Locate every blood parasite and identify its species.
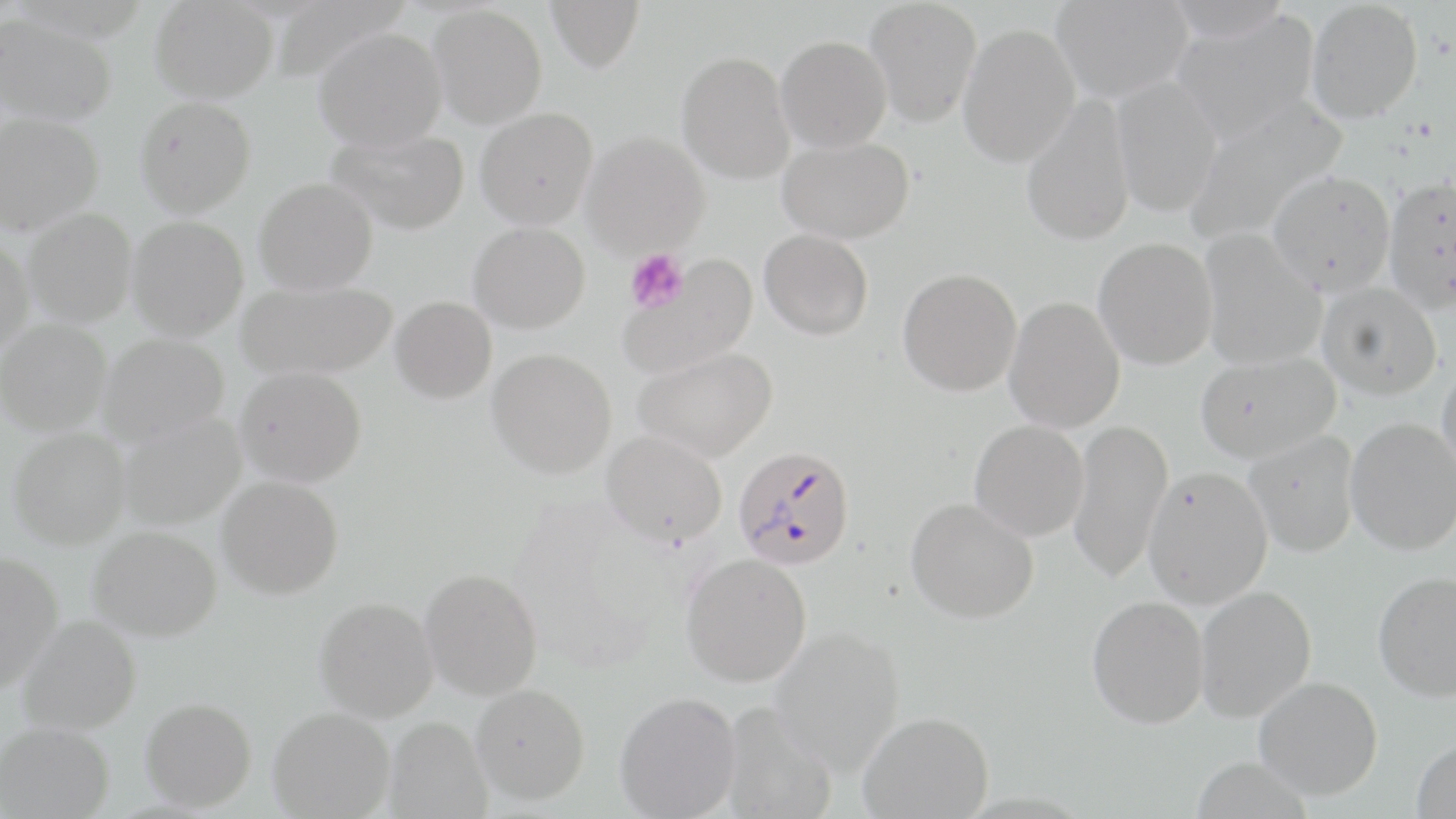

Approximate bounding boxes as [x1, y1, x2, y2] in pixels.
Plasmodium falciparum-infected red blood cells: [733, 445, 855, 570].
No Plasmodium ovale, Plasmodium malariae, Plasmodium vivax, Babesia divergens, or Trypanosoma brucei observed.

Uninfected red blood cell locations: [149, 0, 278, 101], [545, 0, 645, 73], [865, 0, 982, 128], [1052, 0, 1192, 101], [1165, 0, 1293, 41], [1306, 1, 1423, 123], [428, 4, 547, 128], [1171, 9, 1319, 142], [0, 14, 117, 126], [958, 22, 1081, 167], [313, 27, 447, 151], [776, 35, 892, 152], [677, 51, 795, 184], [1111, 77, 1223, 217], [1020, 95, 1136, 247], [135, 96, 256, 217], [1182, 98, 1348, 245], [475, 107, 598, 230], [0, 112, 103, 235], [326, 127, 469, 234], [582, 132, 710, 257], [778, 135, 913, 243], [1267, 169, 1396, 296], [1382, 176, 1456, 313], [254, 177, 378, 294], [24, 209, 138, 327], [127, 216, 249, 340], [468, 222, 590, 333], [759, 229, 873, 340], [1199, 229, 1327, 370], [1093, 237, 1218, 369], [0, 239, 34, 355], [618, 254, 759, 379], [897, 268, 1022, 396], [236, 279, 398, 380], [1316, 282, 1442, 400], [390, 296, 497, 403], [1004, 296, 1126, 433], [0, 319, 112, 436], [99, 334, 229, 445], [633, 346, 777, 461], [487, 349, 617, 478], [1195, 352, 1340, 463], [1437, 357, 1456, 482], [236, 366, 367, 487], [119, 412, 246, 530], [1345, 417, 1456, 555], [1068, 418, 1173, 585], [970, 419, 1089, 540], [7, 427, 130, 549], [603, 431, 727, 546], [1244, 431, 1360, 556], [1144, 466, 1273, 608], [217, 476, 344, 599], [906, 498, 1039, 623], [88, 526, 222, 642], [0, 551, 63, 692], [681, 553, 812, 687], [420, 568, 543, 700], [1372, 571, 1456, 701], [1195, 585, 1316, 722], [1087, 595, 1209, 728], [314, 596, 439, 722], [17, 615, 141, 735], [770, 626, 905, 773], [1255, 676, 1383, 799], [471, 683, 590, 804], [615, 691, 742, 818], [140, 697, 257, 811], [718, 701, 837, 819], [268, 706, 395, 818], [858, 711, 993, 818], [385, 716, 491, 818], [1, 721, 114, 819], [1412, 738, 1456, 819]. Platelet locations: [625, 249, 688, 314]. Slide-level diagnosis: Plasmodium falciparum. Optical microscopy. Image is 1456×819 pixels. May-Grünwald-Giemsa-stained preparation. Thin blood film. Captured at 1000x magnification. One field of a larger specimen.